Locate and identify every blood parasite.
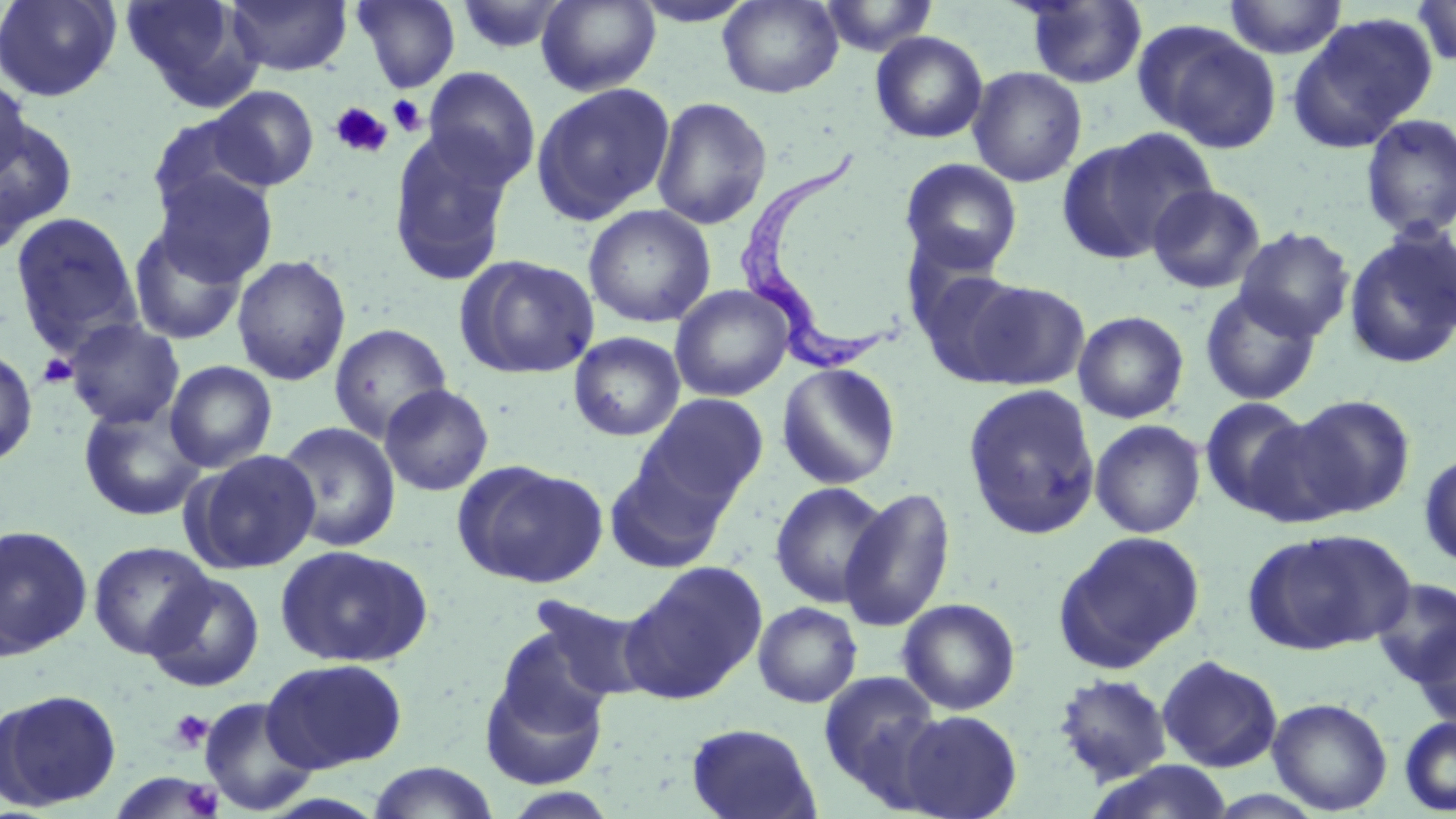

Approximate bounding boxes as (x1, y1, x2, y2) in pixels.
Trypanosoma brucei: (738, 153, 904, 376).
No Plasmodium falciparum, Plasmodium ovale, Plasmodium malariae, Plasmodium vivax, or Babesia divergens observed.

Summary:
  - Platelet locations: (388, 94, 428, 137), (329, 102, 393, 159), (38, 353, 79, 388), (169, 709, 214, 752), (182, 781, 223, 817)
  - Uninfected red blood cell locations: (0, 0, 121, 102), (120, 0, 257, 108), (226, 0, 352, 76), (352, 0, 460, 92), (452, 0, 573, 55), (536, 0, 660, 96), (628, 0, 760, 27), (817, 0, 940, 57), (1223, 0, 1348, 59), (1412, 0, 1456, 68), (718, 1, 843, 98), (1020, 1, 1148, 89), (1286, 14, 1437, 153), (1134, 21, 1281, 153), (870, 31, 988, 144), (423, 67, 541, 189), (967, 67, 1087, 187), (0, 72, 32, 186), (531, 82, 675, 224), (207, 85, 319, 191), (650, 96, 772, 230), (146, 113, 271, 222), (1, 114, 78, 249), (1359, 114, 1456, 239), (1056, 129, 1212, 265), (387, 130, 516, 285), (900, 158, 1022, 274), (153, 170, 277, 288), (1147, 183, 1266, 294), (583, 205, 716, 328), (8, 211, 144, 357), (128, 223, 249, 345), (1234, 226, 1355, 341), (1343, 227, 1456, 370), (232, 254, 351, 386), (455, 254, 600, 380), (911, 263, 1033, 384), (962, 279, 1090, 390), (669, 285, 794, 401), (1199, 288, 1323, 406), (1071, 306, 1321, 418), (1073, 311, 1190, 424), (65, 318, 184, 429), (329, 323, 452, 442), (569, 332, 685, 441), (0, 347, 38, 468), (164, 360, 278, 473), (776, 362, 902, 490), (379, 383, 494, 496), (962, 384, 1101, 540), (638, 393, 769, 509), (1287, 394, 1416, 519), (1199, 396, 1315, 516), (78, 402, 207, 522), (1241, 411, 1359, 530), (1090, 419, 1206, 539), (275, 421, 401, 552), (184, 449, 321, 574), (1418, 452, 1456, 567), (605, 454, 731, 573), (453, 461, 608, 588), (769, 481, 891, 608), (839, 487, 955, 632), (0, 524, 93, 659), (1244, 528, 1413, 655), (1053, 530, 1205, 672), (88, 541, 215, 660), (275, 544, 433, 668), (621, 561, 768, 704), (143, 572, 266, 692), (1371, 578, 1456, 688), (529, 594, 653, 704), (898, 597, 1021, 715), (752, 601, 862, 707), (1412, 625, 1456, 730), (482, 628, 612, 787), (1157, 654, 1283, 773), (262, 658, 409, 773), (819, 671, 943, 798), (1053, 673, 1173, 786), (1, 687, 122, 811), (199, 697, 318, 815), (1267, 697, 1393, 815), (896, 709, 1023, 819), (1399, 716, 1456, 815), (686, 722, 821, 819), (1082, 760, 1236, 819), (366, 762, 499, 819)
  - Slide-level diagnosis: Trypanosoma brucei
  - Preparation: thin blood smear
  - Image size: 1456×819 pixels
  - Magnification: 1000x
  - Field of view: single
  - Stain: May-Grünwald-Giemsa
  - Modality: light microscopy